Report the malaria status of this cell.
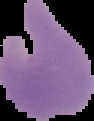
Uninfected.

Summary:
  - Image type: segmented cell region on a black background
  - Image size: 94×121 pixels
  - Preparation: thin blood film